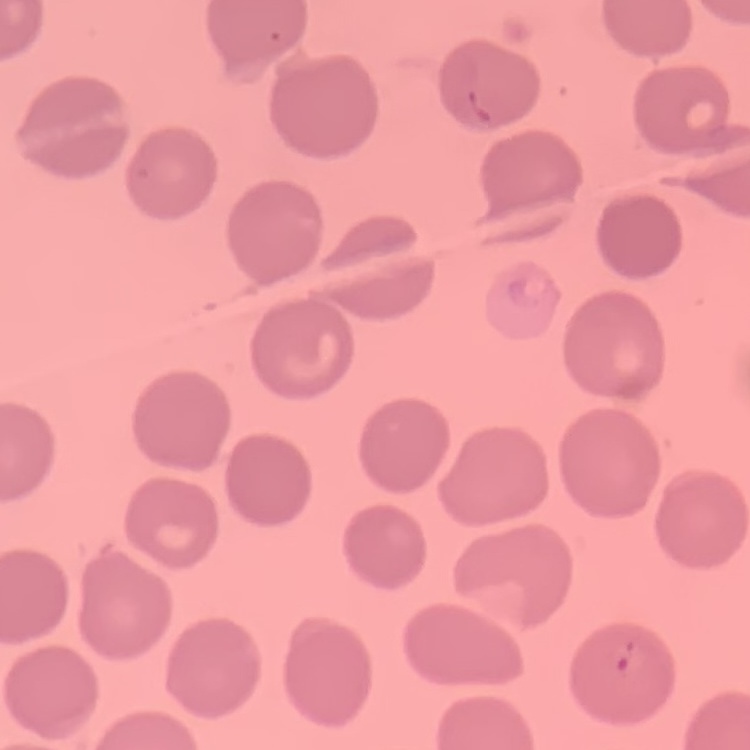

erythrocyte morphology = no rouleaux formation
stain = Field's or Giemsa
preparation = thin blood film
image type = square crop of a larger photomicrograph